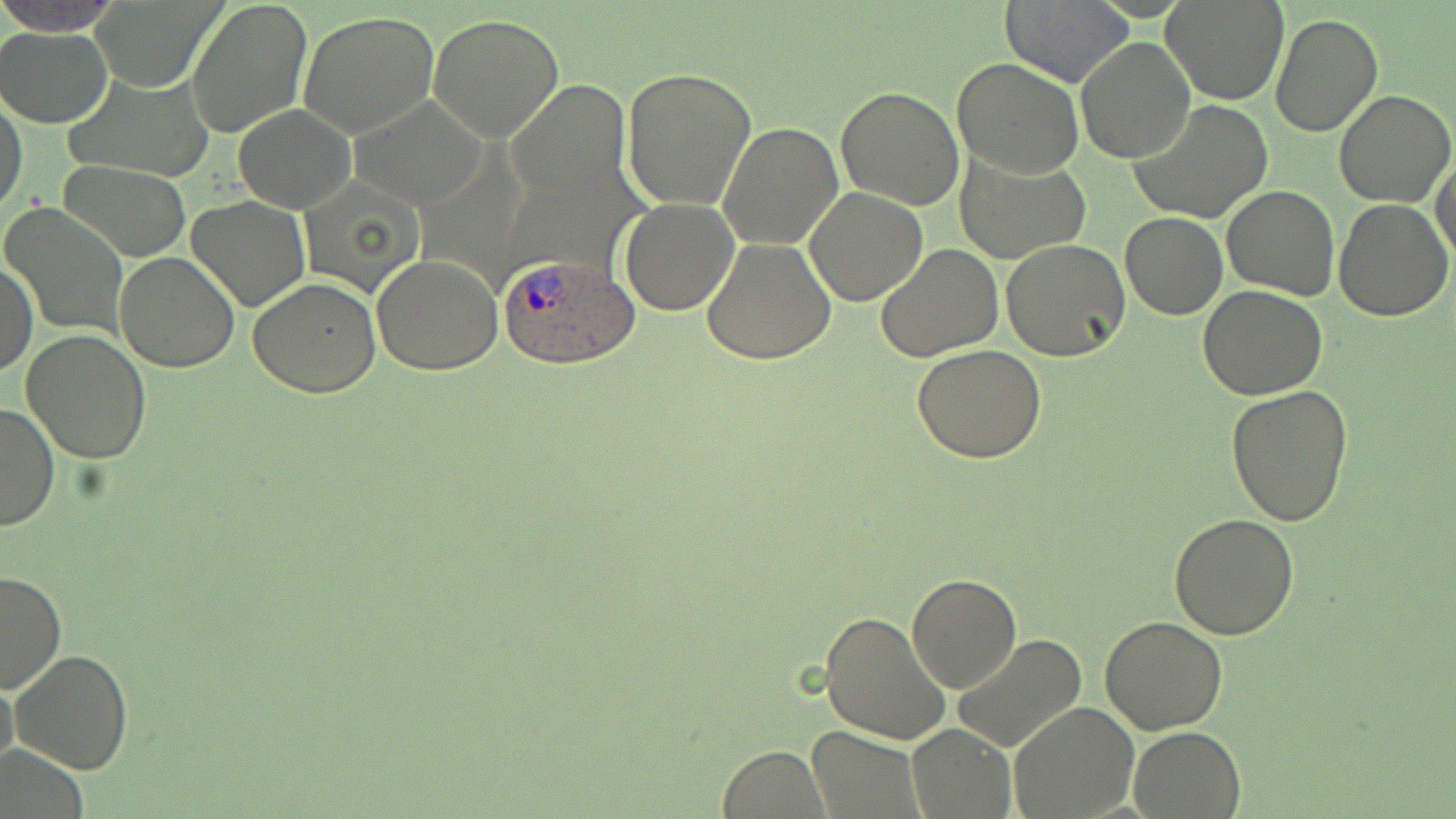
{
  "slide_level_diagnosis": "Plasmodium ovale",
  "modality": "optical microscopy",
  "preparation": "thin blood film",
  "plasmodium_ovale_infected_red_blood_cell_locations": "approximate bounding boxes as (x1,y1)-(x2,y2) corner pairs in pixels: (496,251)-(640,368)",
  "image_size": "1456×819 pixels",
  "uninfected_red_blood_cell_locations": "approximate bounding boxes as (x1,y1)-(x2,y2) corner pairs in pixels: (1,0)-(118,35), (86,0)-(227,91), (185,0)-(312,140), (1000,0)-(1134,88), (1161,1)-(1288,104), (298,9)-(442,140), (428,13)-(565,141), (1269,13)-(1383,137), (1,26)-(116,127), (1076,36)-(1196,163), (952,57)-(1083,178), (620,66)-(758,213), (65,73)-(210,183), (507,79)-(631,201), (836,85)-(965,210), (1332,89)-(1455,209), (1,92)-(28,216), (349,93)-(488,208), (1129,99)-(1275,225), (234,104)-(356,213), (717,121)-(842,249), (954,150)-(1091,263), (1431,153)-(1456,266), (61,161)-(191,262), (302,176)-(426,300), (1222,184)-(1339,300), (804,187)-(929,307), (187,194)-(310,312), (1333,197)-(1453,320), (619,198)-(740,315), (1,204)-(128,338), (1120,212)-(1227,320), (702,237)-(837,367), (1000,238)-(1131,362), (875,244)-(1004,364), (113,252)-(239,373), (371,254)-(503,375), (1,260)-(36,378), (248,278)-(382,398), (1198,285)-(1328,401), (21,328)-(152,464), (912,345)-(1046,464), (1225,384)-(1354,525), (0,401)-(58,533), (1169,515)-(1300,640), (1,571)-(63,695), (905,572)-(1023,693), (820,609)-(951,745), (1098,617)-(1227,735), (950,633)-(1089,754), (10,649)-(131,775), (0,676)-(18,779), (1010,701)-(1139,817), (906,725)-(1015,817), (1128,725)-(1246,817), (806,727)-(924,818), (718,744)-(828,818), (2,747)-(88,818)",
  "magnification": "1000x",
  "field_of_view": "single",
  "stain": "May-Grünwald-Giemsa"
}